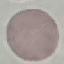

Summary:
  - Result: no malaria parasites seen
  - Preparation: thin blood smear
  - Capture: smartphone through the microscope eyepiece
  - Image type: automatically extracted cell patch, resized to 64 × 64 pixels
  - Stain: Giemsa